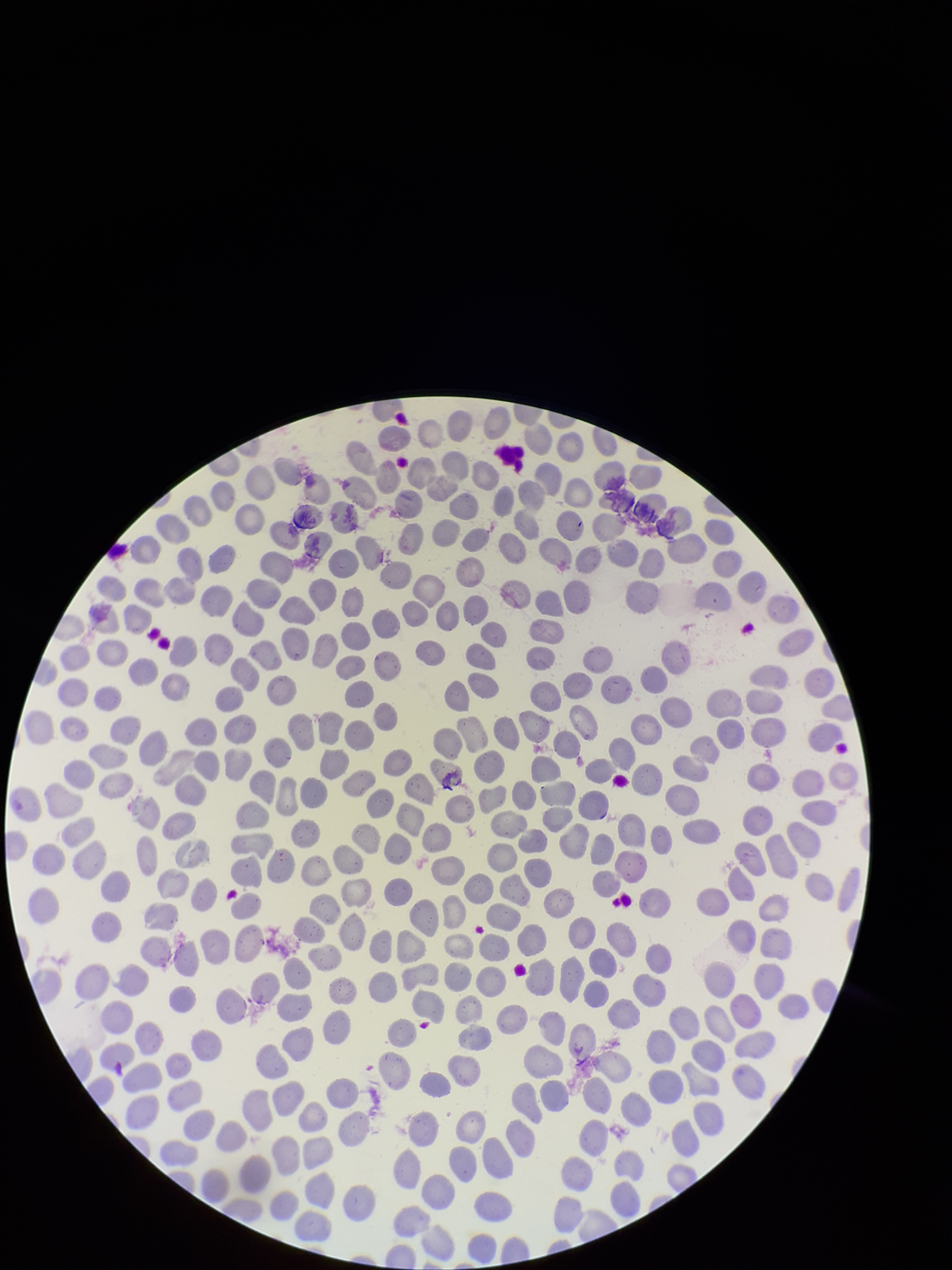
stain = Giemsa
patient malaria status = negative
field of view = single
parasitized red blood cells = none identified
capture = smartphone photograph through the microscope eyepiece
preparation = thin
image size = 952×1270 pixels
red blood cell count = 345
parasitized red blood cell count = 0